Locate every blood parasite and identify its species.
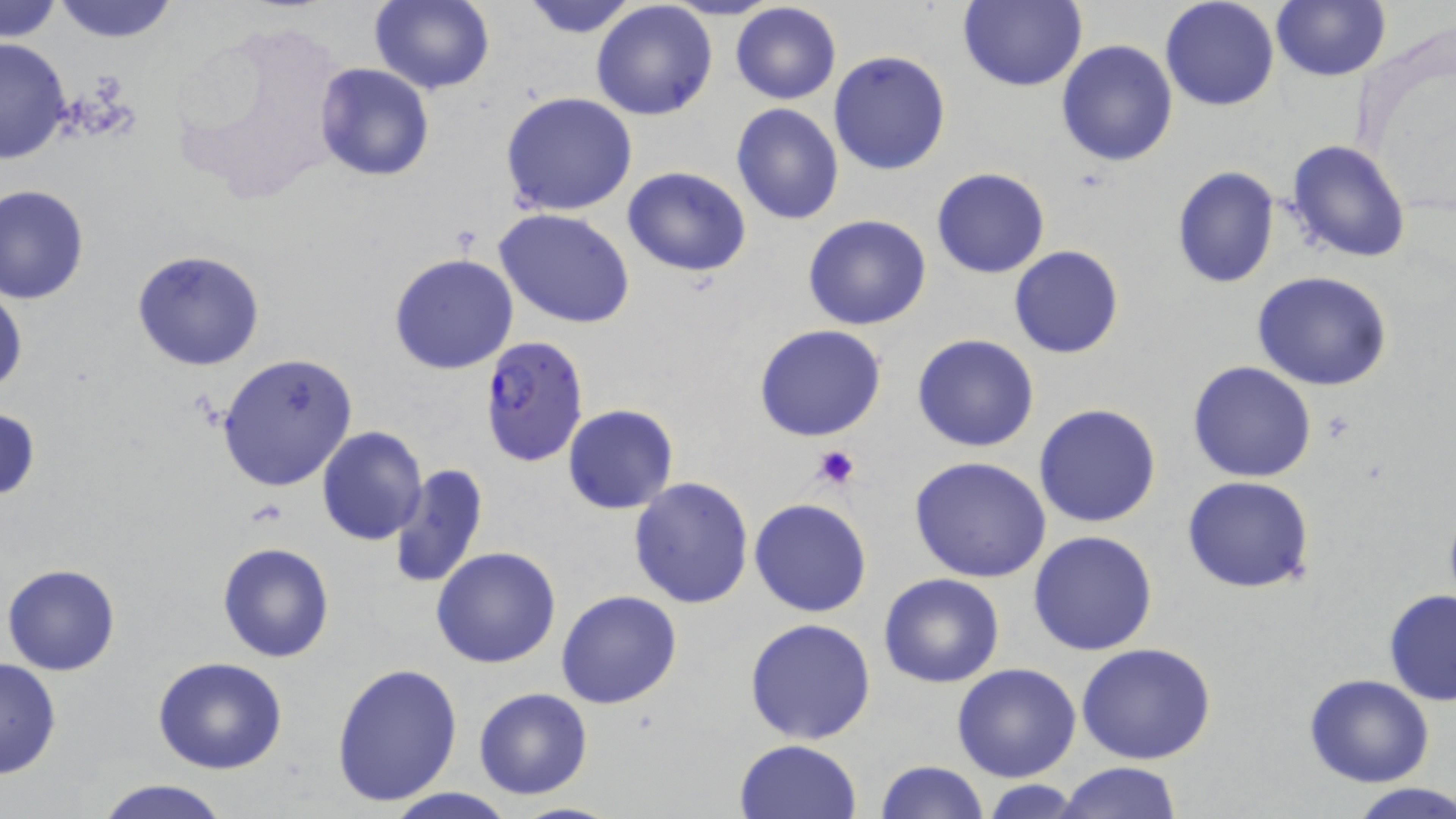

Approximate bounding boxes as (x1, y1, x2, y2) in pixels.
Plasmodium falciparum-infected red blood cells: (479, 334, 589, 468).
No Plasmodium ovale, Plasmodium malariae, Plasmodium vivax, Babesia divergens, or Trypanosoma brucei observed.

Summary:
  - Platelet locations: (810, 444, 861, 493)
  - Uninfected red blood cell locations: (2, 0, 63, 44), (49, 0, 183, 45), (368, 0, 495, 95), (659, 0, 785, 21), (956, 0, 1087, 92), (1160, 0, 1281, 111), (1271, 0, 1390, 81), (519, 1, 642, 39), (590, 2, 719, 120), (729, 2, 842, 105), (165, 10, 358, 212), (0, 37, 73, 164), (1056, 40, 1179, 167), (828, 51, 952, 175), (315, 63, 436, 182), (499, 91, 638, 216), (730, 102, 845, 224), (1286, 139, 1412, 262), (1171, 166, 1280, 289), (622, 167, 751, 277), (931, 168, 1051, 278), (0, 183, 90, 304), (495, 209, 635, 329), (803, 214, 932, 331), (1009, 245, 1125, 360), (132, 249, 266, 371), (389, 252, 518, 374), (1251, 272, 1394, 391), (0, 280, 25, 403), (755, 324, 887, 441), (912, 334, 1040, 453), (217, 352, 358, 491), (1188, 361, 1316, 482), (1033, 403, 1162, 529), (563, 405, 678, 514), (0, 407, 41, 502), (317, 427, 428, 546), (908, 455, 1052, 582), (388, 465, 488, 592), (1181, 475, 1315, 593), (628, 476, 754, 610), (749, 498, 873, 618), (1028, 529, 1159, 655), (216, 540, 336, 663), (431, 546, 562, 668), (3, 563, 121, 676), (878, 573, 1005, 689), (1382, 589, 1456, 706), (555, 590, 683, 709), (744, 617, 876, 743), (1076, 642, 1217, 765), (152, 657, 288, 774), (0, 658, 62, 779), (330, 662, 462, 807), (952, 662, 1082, 783), (1304, 673, 1435, 787), (472, 686, 594, 800), (733, 739, 863, 819), (874, 760, 987, 818), (1057, 761, 1183, 818), (94, 778, 233, 819), (980, 779, 1086, 817), (1345, 781, 1456, 819), (380, 788, 519, 819), (505, 800, 634, 819)
  - Slide-level diagnosis: Plasmodium falciparum
  - Magnification: 1000x
  - Preparation: thin blood smear
  - Stain: May-Grünwald-Giemsa
  - Modality: light microscopy
  - Image size: 1456×819 pixels
  - Field of view: single